Name the parasite shown.
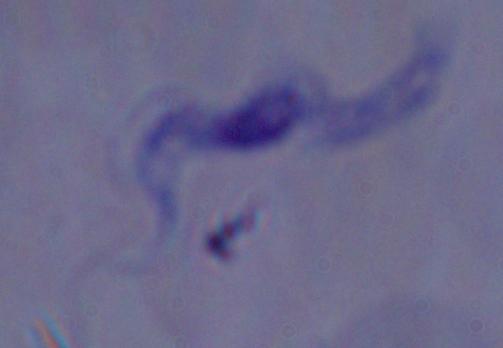
A trypanosome.

magnification = 1000x
modality = photomicrograph